Comment on the morphology of the erythrocytes.
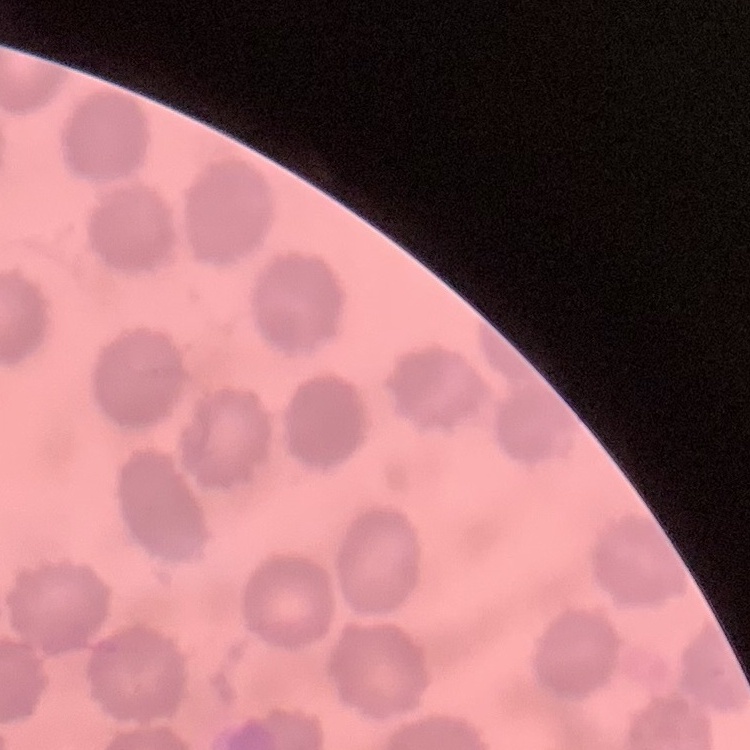

They show no rouleaux formation.

stain = Field's or Giemsa
preparation = thin peripheral smear
image type = one tile cut from a larger photomicrograph